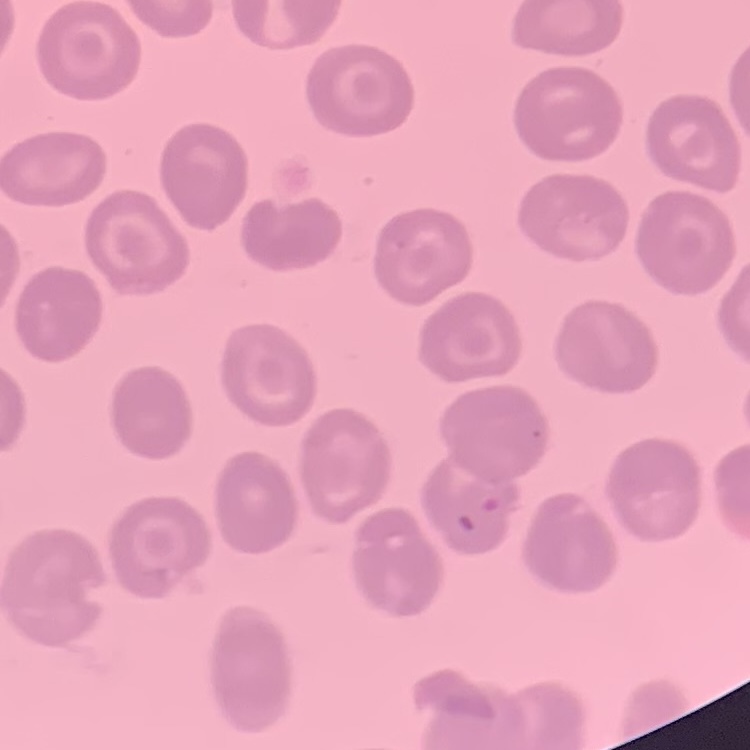
Summary:
  - Erythrocyte morphology: no rouleaux formation
  - Image type: square crop of a larger photomicrograph
  - Stain: Field's or Giemsa
  - Preparation: thin blood film